Assess the morphology of the erythrocytes.
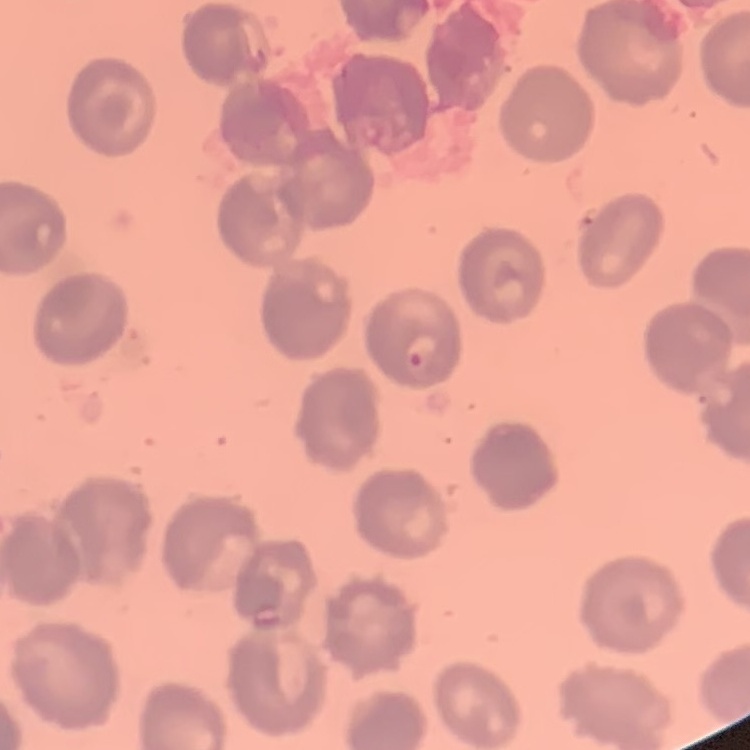
They show no rouleaux formation.

Thin blood film. Stained with either Field's or Giemsa. Square crop of a larger photomicrograph.